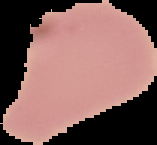

Image is 157×145 pixels. The area outside the segmented cell region is set to black. From a thin blood smear. Result: no malaria parasites detected.